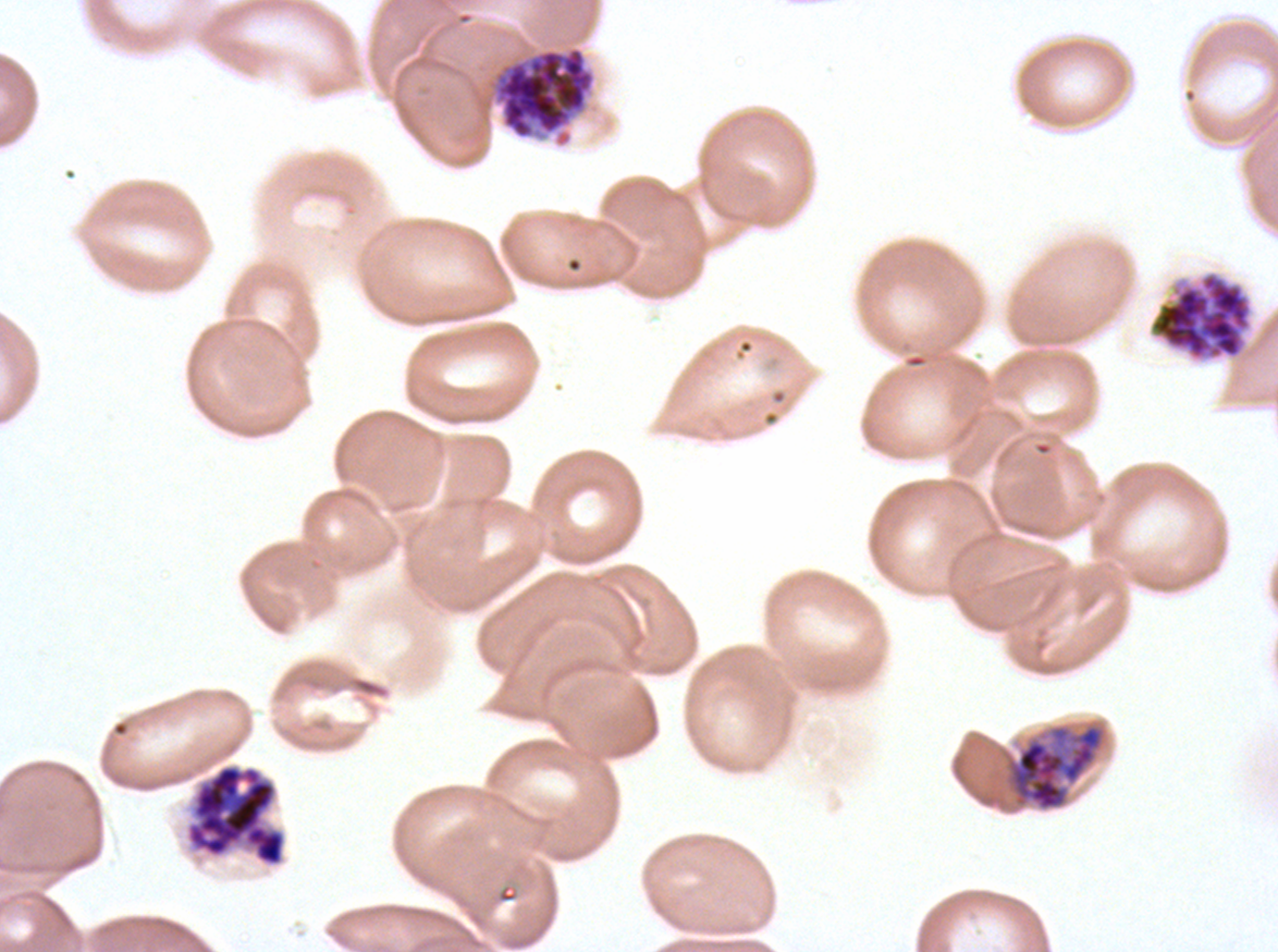

Approximate bounding boxes as (x1, y1, x2, y2) in pixels.
Summary:
  - Early schizont locations: (1005, 723, 1106, 812)
  - Segmenter locations: (183, 762, 288, 869)
  - Late schizont locations: (493, 45, 596, 147), (1148, 269, 1254, 363)
  - Image size: 1278×952 pixels
  - Field of view: sub-image separated from a larger composite
  - Preparation: thin blood smear
  - Specimen: ex-vivo Plasmodium falciparum culture from a patient in The Gambia, grown for 24 to 48 hours
  - Life-cycle stages observed: early schizont, late schizont, segmenter
  - Stain: Giemsa